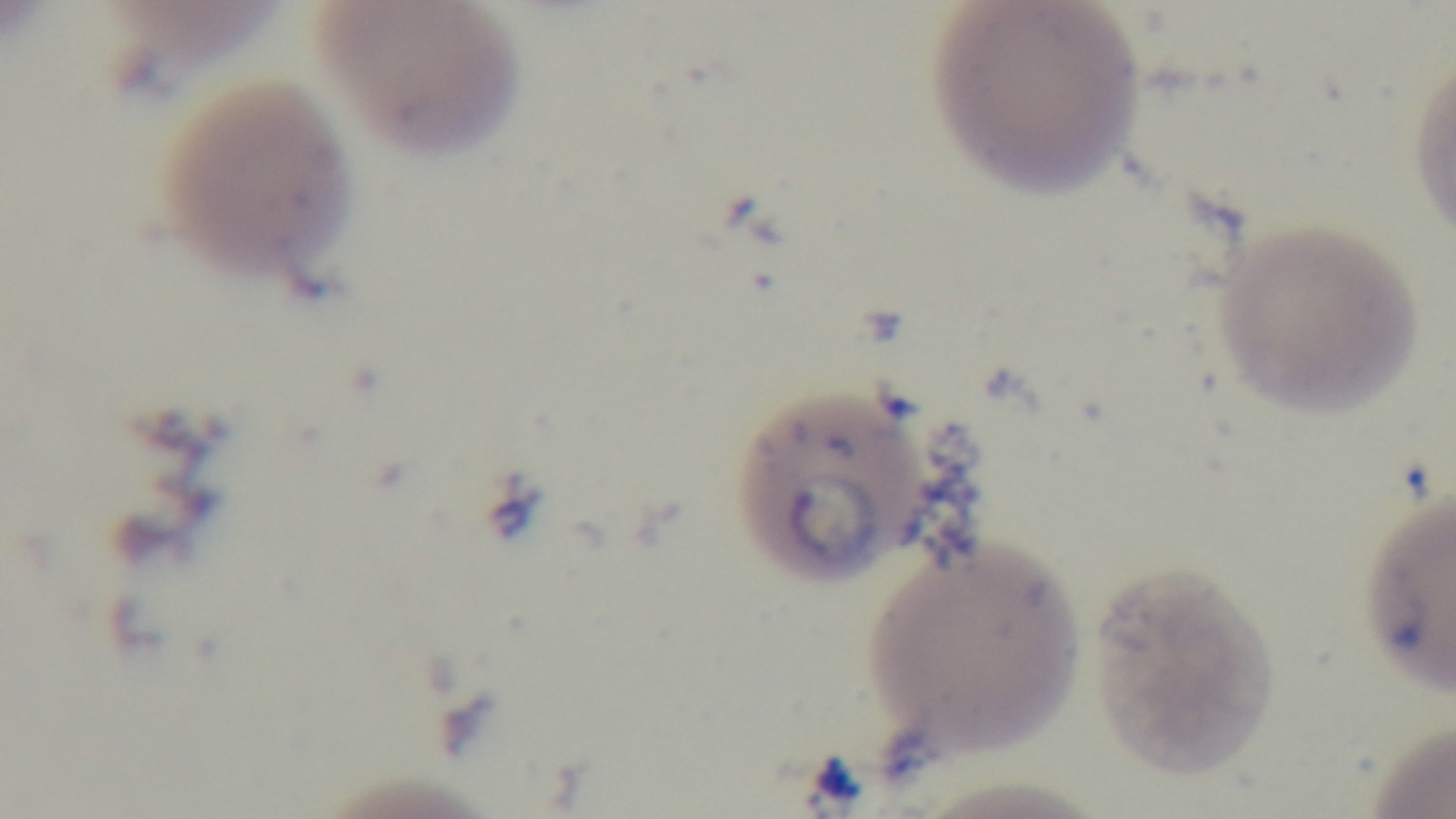

capture = mounted 4K digital camera
field of view = single
stain = Giemsa
modality = light microscopy
preparation = thin
malaria status = positive
objective = 100x oil immersion